Assess the morphology of the red blood cells.
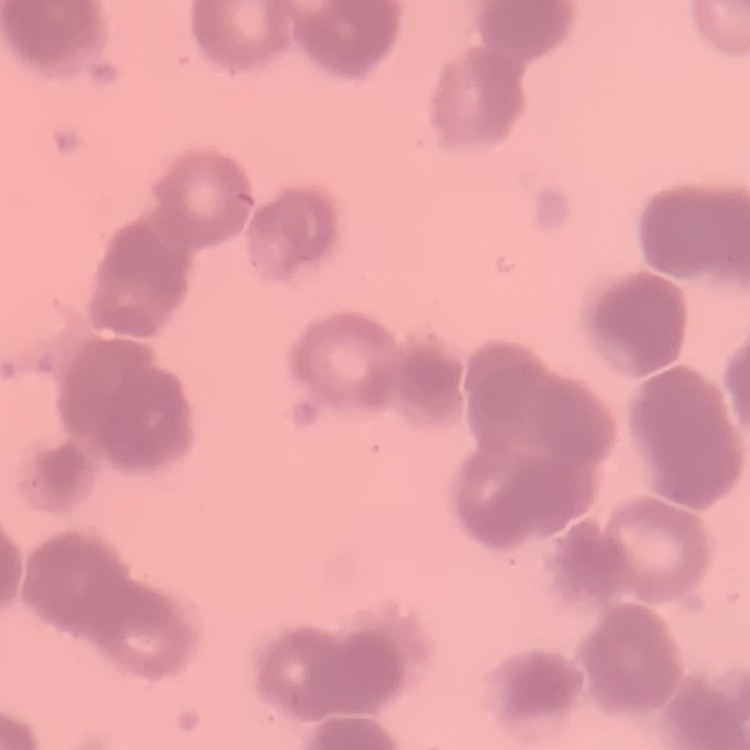

They show rouleaux formation.

Summary:
  - Stain: Field's or Giemsa
  - Image type: square crop of a larger photomicrograph
  - Preparation: thin blood smear